Name the parasite shown.
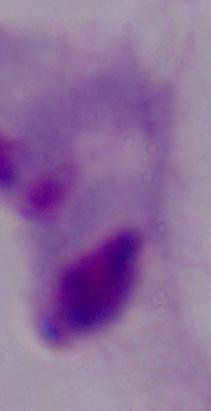

A trichomonad.

magnification = 1000x
modality = photomicrograph